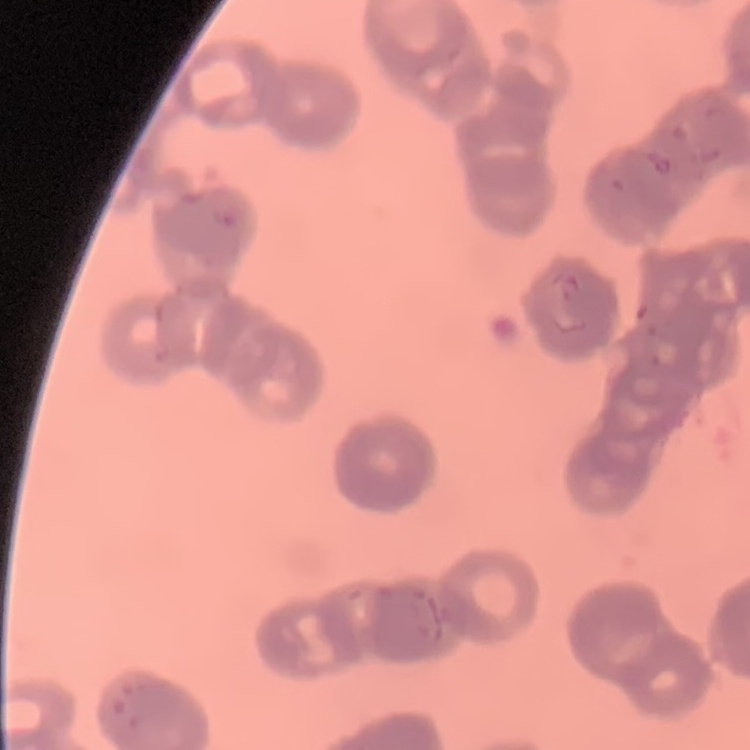
red blood cell morphology = rouleaux formation
preparation = thin blood smear
stain = Field's or Giemsa
image type = one tile cut from a larger photomicrograph